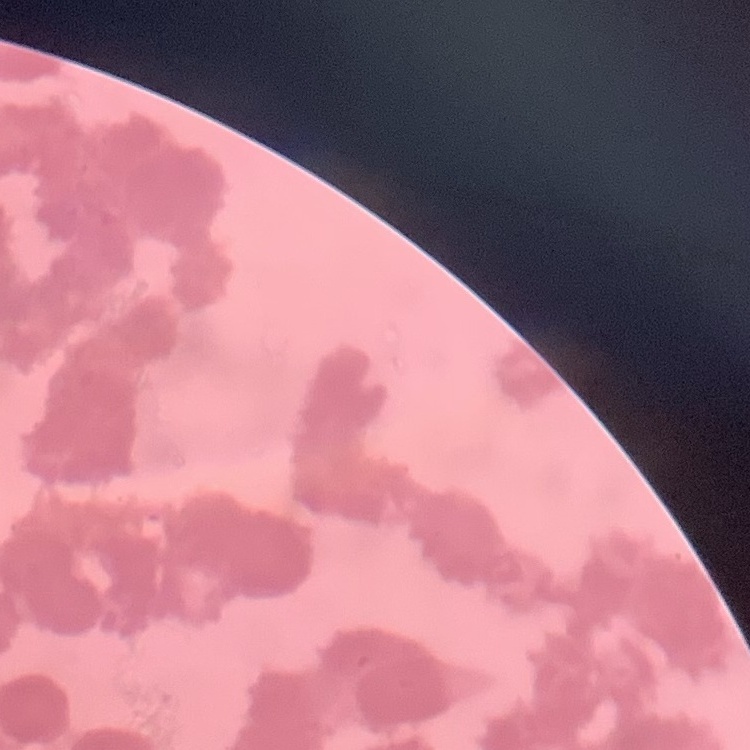
Summary:
  - Red blood cell morphology: rouleaux formation
  - Preparation: thin blood smear
  - Stain: Field's or Giemsa
  - Image type: one tile cut from a larger photomicrograph